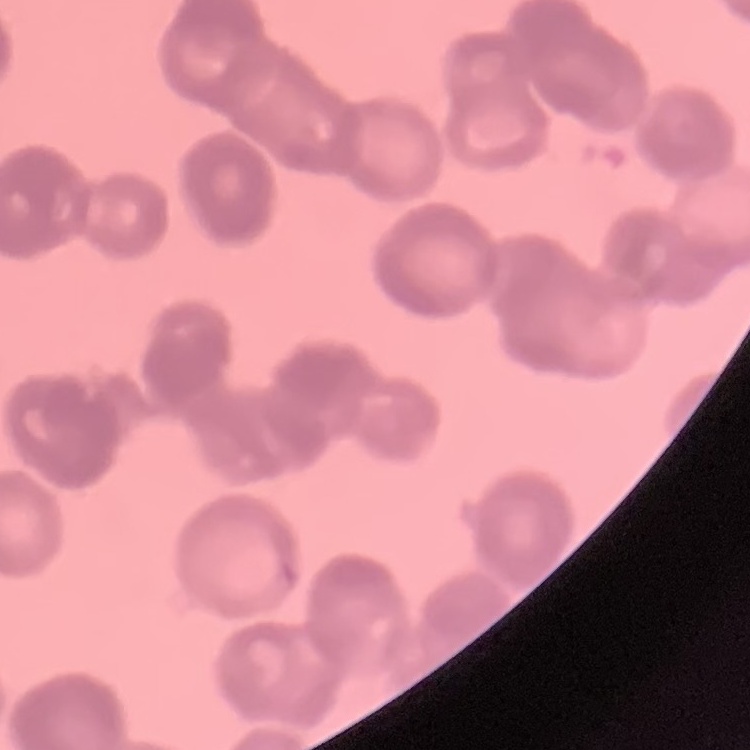

Summary:
  - Erythrocyte morphology: rouleaux formation
  - Image type: square crop of a larger photomicrograph
  - Stain: Field's or Giemsa
  - Preparation: thin peripheral smear